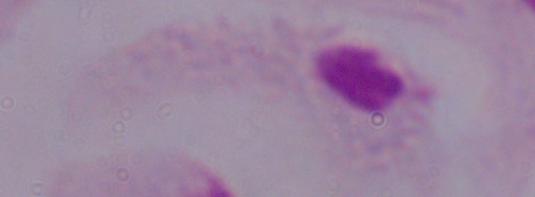

Summary:
  - Modality: photomicrograph
  - Identification: trichomonad
  - Magnification: 1000x